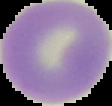
From a thin blood film. Image is 112×106 pixels. Malaria status: uninfected. Segmented cell region on a black background.